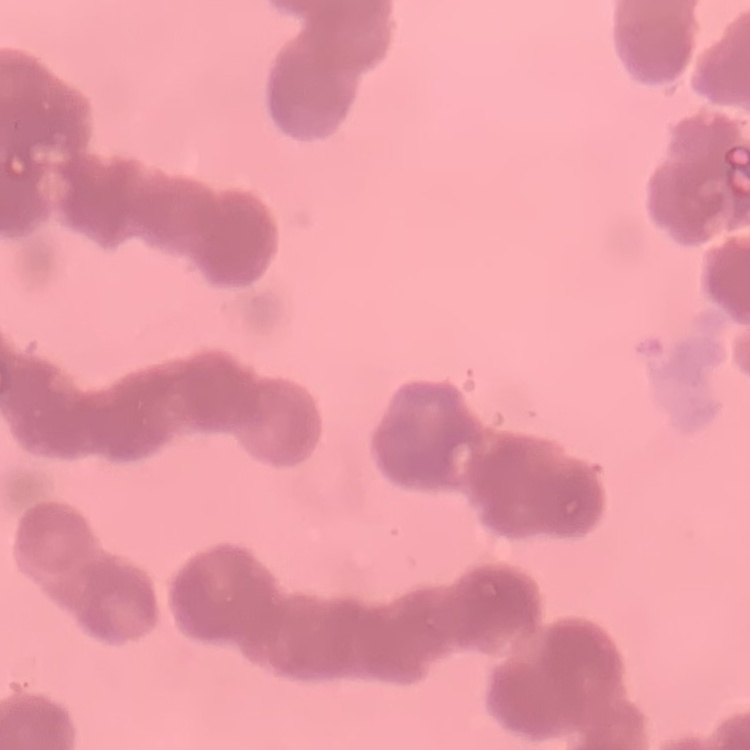
red blood cell morphology = rouleaux formation
image type = square crop of a larger photomicrograph
stain = Field's or Giemsa
preparation = thin peripheral smear